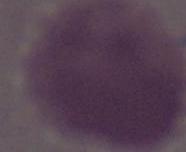 Photomicrograph. 1000x magnification. An erythrocyte is seen.